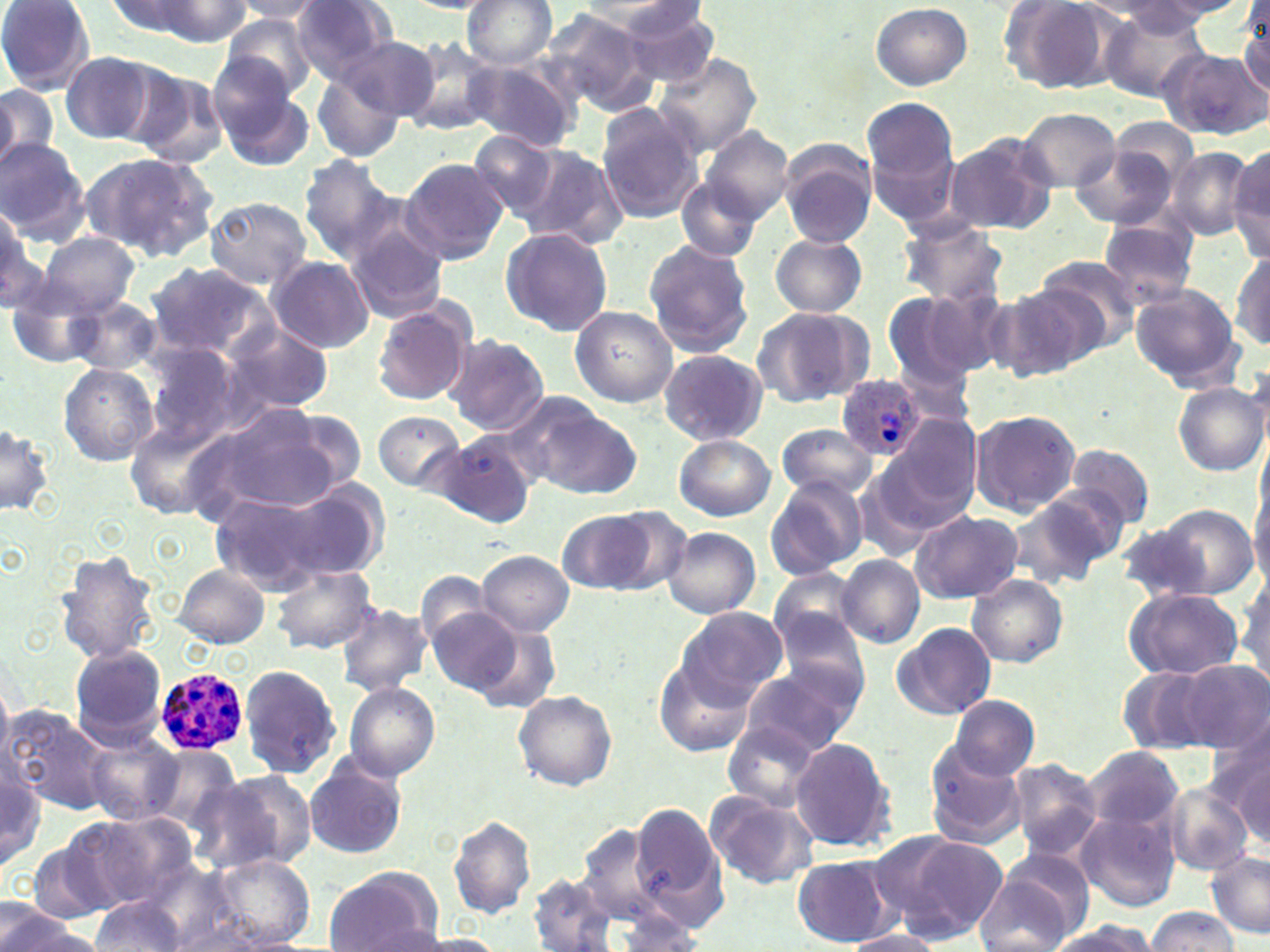

Summary:
  - Coordinate format: approximate bounding boxes as (x1,y1)-(x2,y2) corner pairs in pixels
  - Uninfected red blood cell locations: (0,0)-(95,92), (104,0)-(208,40), (144,0)-(253,44), (287,0)-(397,84), (461,0)-(559,69), (1002,0)-(1119,95), (230,1)-(328,23), (404,1)-(497,13), (563,1)-(694,24), (582,1)-(711,51), (1114,1)-(1247,34), (870,3)-(972,89), (1236,4)-(1269,100), (618,5)-(722,88), (1100,5)-(1211,103), (538,6)-(657,118), (218,13)-(320,100), (335,32)-(441,124), (401,36)-(502,138), (1161,49)-(1267,141), (59,51)-(162,144), (654,53)-(761,155), (465,58)-(582,153), (212,64)-(313,169), (125,65)-(229,168), (312,67)-(408,164), (0,84)-(56,170), (862,100)-(962,226), (595,104)-(705,224), (1017,108)-(1121,191), (1105,115)-(1201,192), (698,125)-(794,226), (469,131)-(561,221), (944,133)-(1056,234), (0,140)-(90,243), (517,146)-(629,250), (778,146)-(878,249), (1070,147)-(1177,229), (1167,148)-(1255,239), (1227,149)-(1270,257), (81,151)-(221,264), (297,155)-(401,264), (399,158)-(509,265), (677,179)-(762,262), (203,195)-(312,291), (0,200)-(45,312), (1097,215)-(1201,311), (896,216)-(1009,309), (345,223)-(450,323), (499,227)-(613,335), (38,231)-(139,317), (770,234)-(866,319), (643,238)-(755,357), (1231,252)-(1270,351), (1033,253)-(1144,350), (268,255)-(374,353), (144,263)-(274,362), (1001,280)-(1109,378), (9,282)-(103,369), (1131,286)-(1242,388), (881,290)-(989,393), (67,296)-(162,376), (371,303)-(474,406), (570,305)-(678,406), (750,305)-(873,408), (225,322)-(332,415), (445,334)-(550,435), (141,344)-(240,450), (658,349)-(767,446), (59,364)-(157,466), (1173,380)-(1268,476), (513,395)-(641,500), (196,400)-(347,520), (274,407)-(370,496), (372,409)-(468,495), (967,410)-(1081,517), (876,413)-(983,528), (125,419)-(225,519), (0,420)-(55,518), (776,423)-(878,503), (429,434)-(540,526), (674,434)-(775,521), (1065,443)-(1155,530), (1250,470)-(1270,589), (764,475)-(869,579), (210,482)-(370,590), (1010,487)-(1126,587), (1150,502)-(1259,600), (557,509)-(658,594), (910,509)-(1021,603), (1115,523)-(1215,603), (663,527)-(761,619), (475,549)-(574,637), (56,551)-(161,663), (836,555)-(923,649), (273,565)-(378,654), (174,566)-(271,647), (769,566)-(862,654), (1236,566)-(1269,688), (415,568)-(493,655), (967,574)-(1067,668), (1123,587)-(1245,680), (334,602)-(434,695), (770,604)-(870,703), (427,605)-(523,694), (676,606)-(788,705), (890,622)-(997,721), (471,623)-(562,714), (69,645)-(168,746), (652,657)-(754,757), (1175,661)-(1269,754), (240,664)-(342,780), (739,665)-(859,758), (1118,665)-(1225,755), (343,681)-(440,782), (514,690)-(618,791), (947,695)-(1039,781), (3,706)-(112,815), (1210,719)-(1270,835), (720,722)-(822,812), (84,731)-(183,826), (789,736)-(896,852), (925,744)-(1030,850), (149,745)-(241,829), (1084,747)-(1182,833), (1230,749)-(1268,847), (0,753)-(44,876), (303,755)-(410,860), (1006,757)-(1105,863), (212,768)-(318,871), (1162,783)-(1254,877), (704,790)-(820,890), (626,799)-(728,929), (76,811)-(202,912), (1075,811)-(1181,913), (449,816)-(537,921), (572,821)-(669,930), (869,830)-(1005,944), (29,835)-(115,924), (1205,852)-(1270,938), (791,855)-(896,947), (214,856)-(313,945), (976,857)-(1088,952), (323,867)-(442,952), (529,873)-(620,952), (90,897)-(188,951), (0,902)-(83,952), (1144,907)-(1241,951), (1046,921)-(1158,952), (844,929)-(946,951)
  - Plasmodium ovale-infected red blood cell locations: (839,376)-(926,461), (152,666)-(248,754)
  - Slide-level diagnosis: Plasmodium ovale
  - Field of view: one of a larger specimen
  - Image size: 1270×952 pixels
  - Stain: May-Grünwald-Giemsa
  - Magnification: 1000x
  - Modality: optical microscopy
  - Preparation: thin blood film